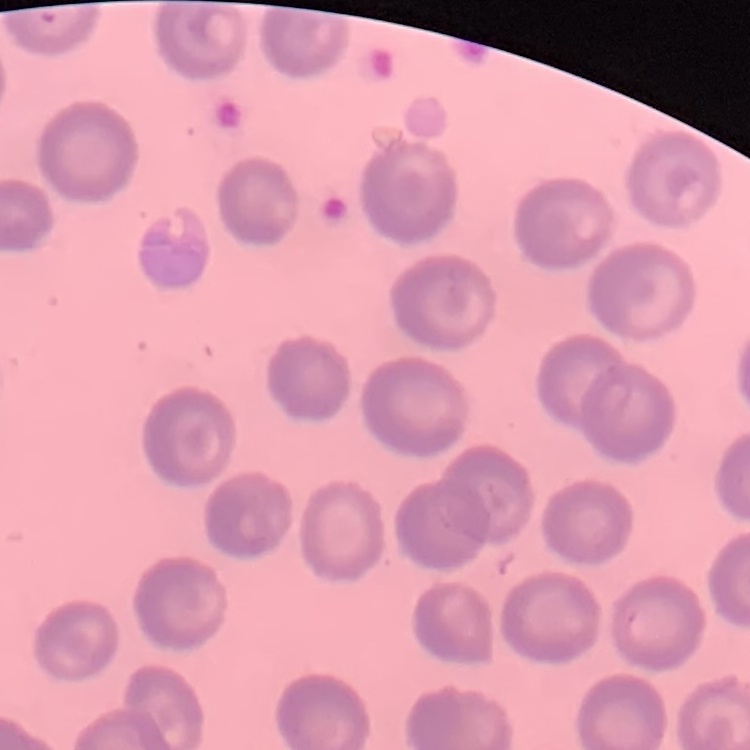
Summary:
  - Erythrocyte morphology: no rouleaux formation
  - Stain: Field's or Giemsa
  - Image type: square crop of a larger photomicrograph
  - Preparation: thin blood film